Locate and identify every blood parasite.
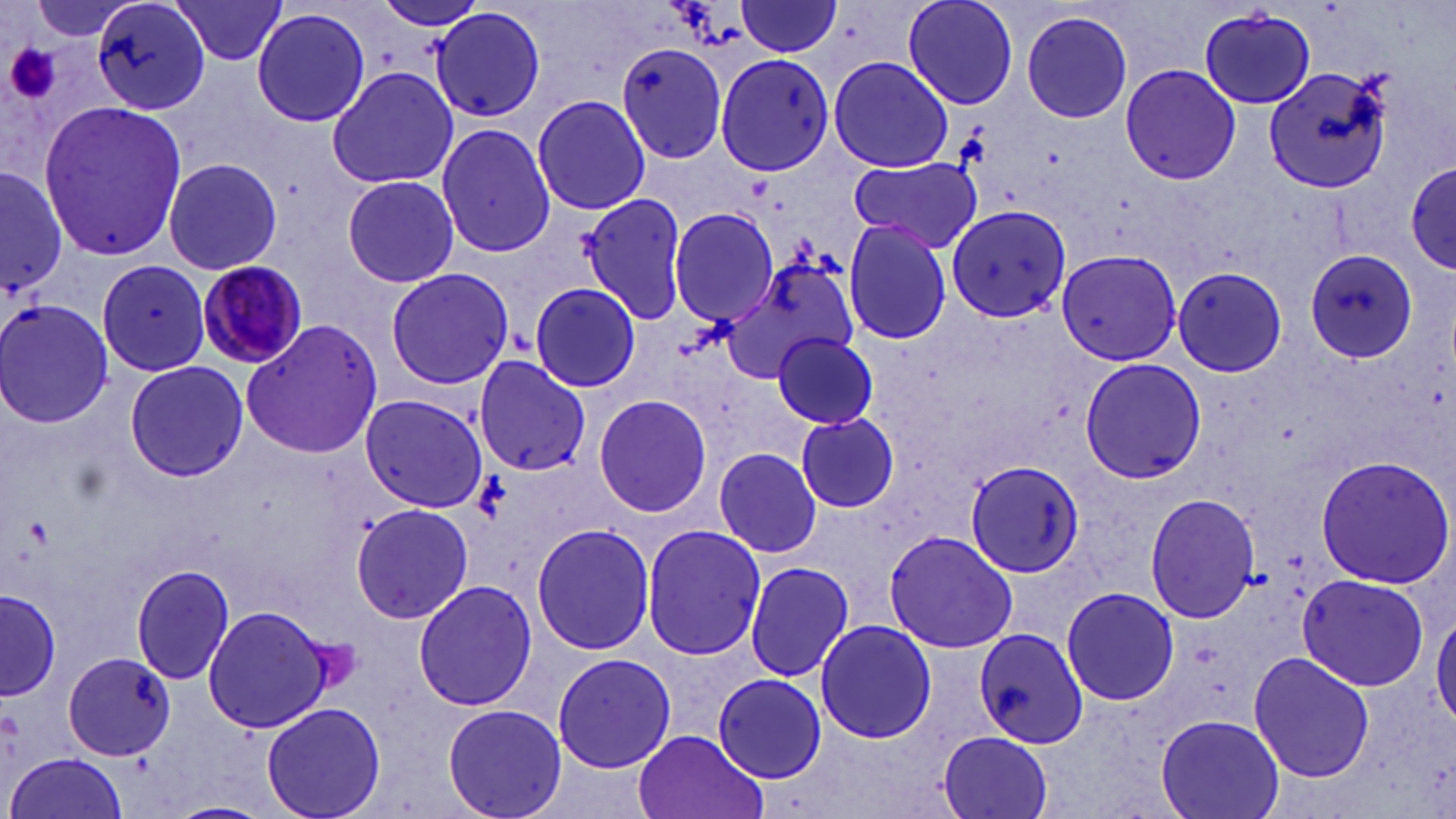

Approximate bounding boxes as (x1,y1)-(x2,y2) corner pairs in pixels.
Plasmodium malariae-infected red blood cells: (193,257)-(310,369).
No Plasmodium falciparum, Plasmodium ovale, Plasmodium vivax, Babesia divergens, or Trypanosoma brucei observed.

Uninfected red blood cell locations: (90,0)-(210,114), (374,0)-(486,30), (901,0)-(1019,110), (168,1)-(291,67), (735,2)-(844,57), (250,7)-(371,129), (430,7)-(547,124), (1196,9)-(1318,108), (1020,10)-(1133,124), (616,43)-(731,171), (714,51)-(836,174), (828,54)-(954,171), (325,64)-(459,192), (1266,64)-(1395,193), (1119,65)-(1241,184), (531,95)-(652,214), (37,99)-(189,260), (436,123)-(555,256), (846,155)-(983,253), (163,157)-(282,277), (1405,158)-(1454,274), (0,169)-(70,308), (339,176)-(460,289), (576,192)-(695,324), (957,204)-(1077,325), (668,206)-(778,326), (842,220)-(952,345), (1055,248)-(1183,365), (1303,248)-(1419,362), (731,256)-(861,377), (96,262)-(213,374), (385,266)-(514,390), (1169,266)-(1287,377), (530,281)-(641,393), (2,298)-(114,429), (242,318)-(383,460), (771,331)-(882,431), (472,355)-(589,476), (1080,356)-(1206,486), (124,361)-(249,483), (592,392)-(715,519), (360,394)-(487,512), (794,411)-(900,515), (713,448)-(823,557), (1315,455)-(1455,588), (963,459)-(1088,576), (1144,492)-(1260,623), (349,502)-(476,625), (530,523)-(655,656), (639,524)-(766,662), (883,529)-(1020,654), (742,559)-(854,682), (130,565)-(237,685), (1297,574)-(1429,692), (413,579)-(539,711), (1060,586)-(1178,707), (2,587)-(59,702), (202,603)-(333,735), (1432,610)-(1456,732), (815,619)-(937,744), (973,628)-(1089,752), (61,650)-(176,761), (553,650)-(675,773), (1248,650)-(1377,783), (713,672)-(827,783), (262,701)-(386,819), (442,703)-(565,819), (1155,711)-(1285,819), (632,729)-(765,819), (937,731)-(1054,819), (6,751)-(128,819). Platelet locations: (3,40)-(63,107). Slide-level diagnosis: Plasmodium malariae. Captured at 1000x magnification. Thin blood smear. May-Grünwald-Giemsa stain. Light microscopy. One field of a larger specimen. Image is 1456×819 pixels.